Outline each blood parasite and name the species.
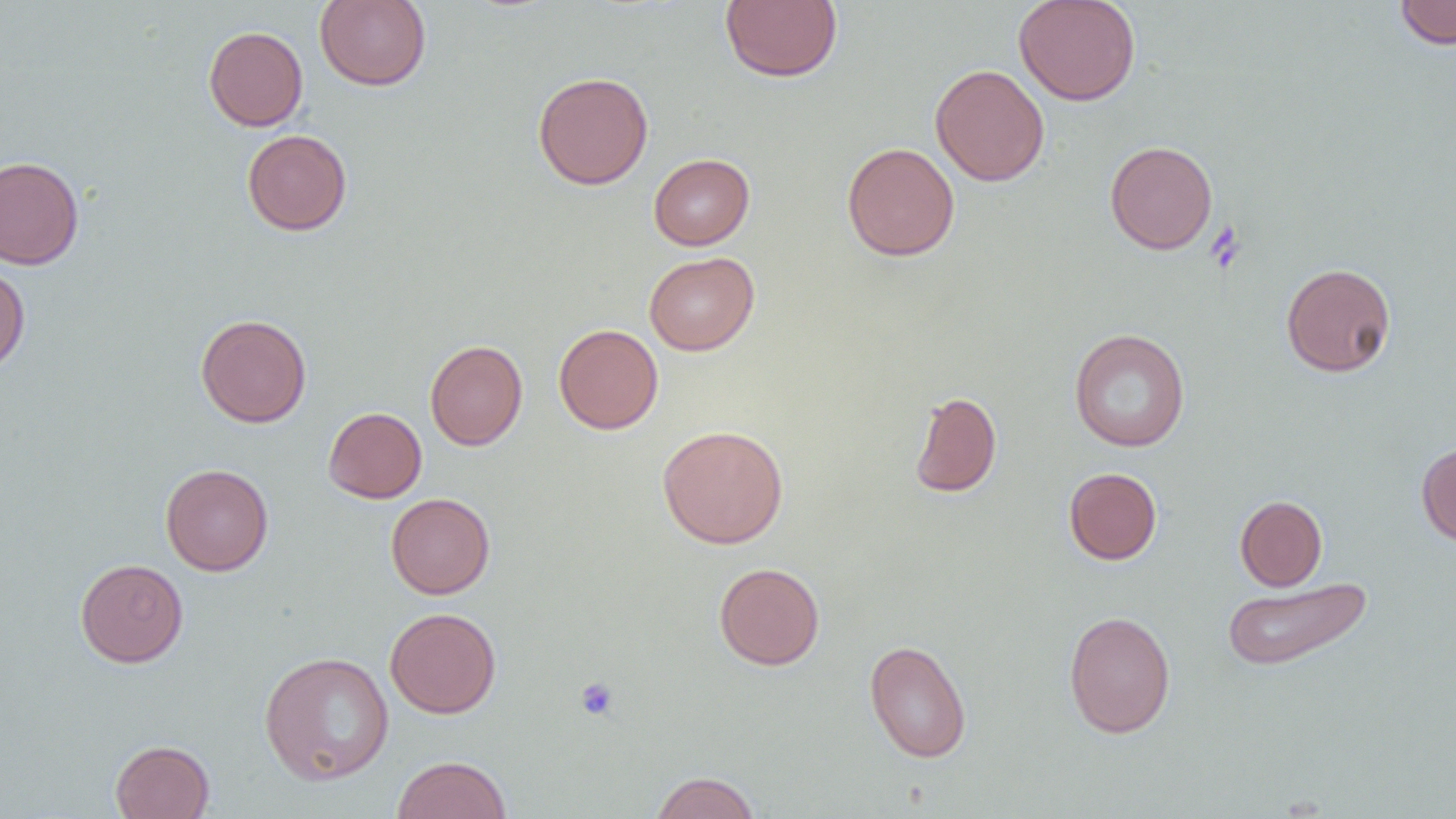
No blood parasites seen.

Summary:
  - Coordinate format: approximate bounding boxes as named x1/y1/x2/y2 corners in pixels
  - Uninfected red blood cell locations: (x1=315, y1=0, x2=431, y2=91), (x1=720, y1=0, x2=842, y2=83), (x1=1013, y1=0, x2=1141, y2=106), (x1=1394, y1=0, x2=1456, y2=50), (x1=203, y1=25, x2=308, y2=131), (x1=930, y1=64, x2=1049, y2=187), (x1=532, y1=71, x2=654, y2=190), (x1=242, y1=129, x2=352, y2=235), (x1=1105, y1=140, x2=1218, y2=254), (x1=842, y1=142, x2=960, y2=261), (x1=648, y1=153, x2=755, y2=250), (x1=0, y1=155, x2=84, y2=270), (x1=644, y1=252, x2=759, y2=355), (x1=1280, y1=262, x2=1397, y2=377), (x1=0, y1=263, x2=30, y2=374), (x1=195, y1=314, x2=312, y2=427), (x1=553, y1=324, x2=664, y2=434), (x1=1069, y1=328, x2=1190, y2=452), (x1=425, y1=339, x2=528, y2=450), (x1=909, y1=391, x2=1002, y2=498), (x1=323, y1=407, x2=427, y2=503), (x1=657, y1=424, x2=789, y2=548), (x1=1416, y1=441, x2=1456, y2=547), (x1=160, y1=463, x2=273, y2=576), (x1=1063, y1=467, x2=1162, y2=565), (x1=386, y1=493, x2=495, y2=599), (x1=1235, y1=495, x2=1327, y2=591), (x1=75, y1=558, x2=188, y2=668), (x1=713, y1=562, x2=825, y2=670), (x1=1221, y1=577, x2=1373, y2=672), (x1=385, y1=607, x2=501, y2=718), (x1=1063, y1=610, x2=1176, y2=738), (x1=864, y1=639, x2=972, y2=762), (x1=259, y1=651, x2=394, y2=784), (x1=110, y1=740, x2=214, y2=818), (x1=392, y1=755, x2=512, y2=819), (x1=649, y1=771, x2=761, y2=818)
  - Platelet locations: (x1=1206, y1=220, x2=1247, y2=274), (x1=575, y1=677, x2=619, y2=721)
  - Slide-level diagnosis: negative for blood parasites
  - Magnification: 1000x
  - Modality: light microscopy
  - Image size: 1456×819 pixels
  - Field of view: single
  - Preparation: thin blood film